Give the position of every malaria parasite.
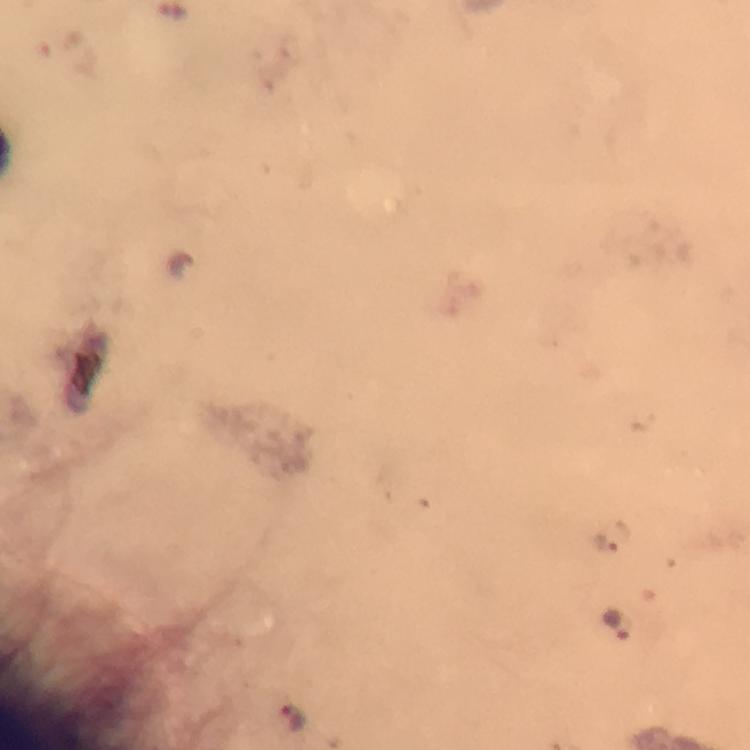
Approximate centers as {x, y} in pixels.
Malaria parasites: {608, 542}, {617, 626}, {292, 717}.

Giemsa stain. Immersion oil applied. Photographed through the microscope with a smartphone camera. Cropped region of a single field of view. From a malaria diagnostic workup. Thick smear. 100x magnification. Image is 750×750 pixels.